Locate every blood parasite and identify its species.
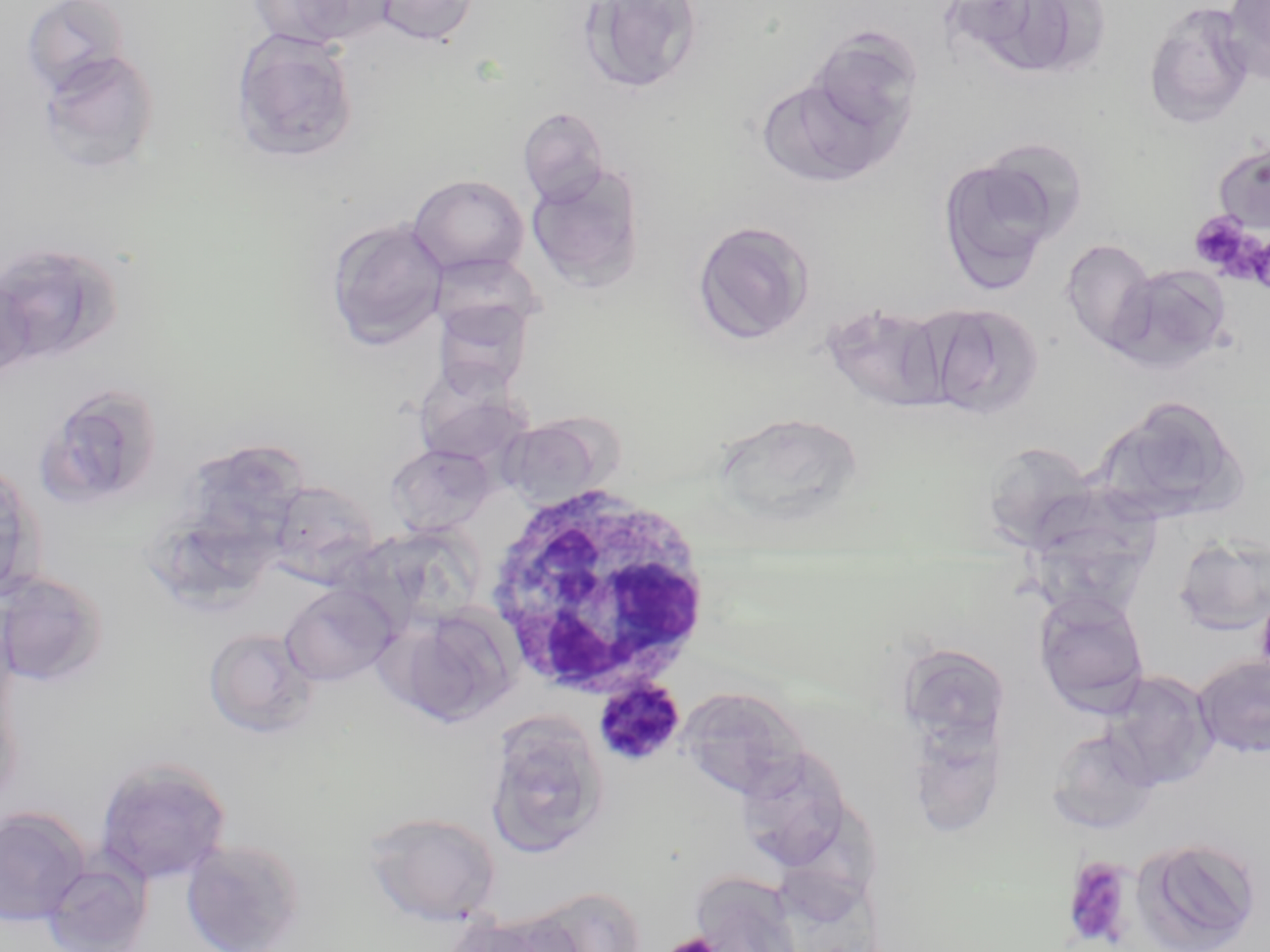
Approximate bounding boxes as (x1,y1)-(x2,y2) corner pairs in pixels.
Plasmodium malariae-infected red blood cells: (593,680)-(685,768).
No Plasmodium falciparum, Plasmodium ovale, Plasmodium vivax, Babesia divergens, or Trypanosoma brucei observed.

Uninfected red blood cell locations: (22,0)-(130,96), (251,0)-(394,49), (374,0)-(479,45), (579,0)-(705,95), (1221,0)-(1270,83), (1144,3)-(1255,128), (231,27)-(360,164), (805,29)-(923,142), (38,49)-(160,174), (757,75)-(902,189), (518,106)-(609,205), (979,136)-(1090,243), (1212,140)-(1270,234), (937,157)-(1059,294), (526,163)-(646,292), (408,174)-(529,277), (326,218)-(448,349), (692,219)-(815,345), (1060,238)-(1157,353), (0,241)-(124,365), (428,252)-(544,341), (1108,263)-(1234,374), (0,277)-(36,382), (432,298)-(535,397), (919,301)-(1046,420), (822,302)-(951,414), (36,382)-(164,509), (1094,395)-(1248,526), (503,417)-(607,509), (179,438)-(312,557), (979,441)-(1100,552), (387,443)-(494,535), (0,458)-(45,601), (265,480)-(381,584), (1172,534)-(1270,637), (0,571)-(109,687), (280,583)-(396,686), (1032,589)-(1151,718), (391,606)-(519,727), (203,627)-(317,737), (897,643)-(1012,751), (1193,653)-(1270,757), (1101,670)-(1218,790), (677,686)-(809,802), (907,707)-(1010,842), (483,711)-(610,859), (1046,727)-(1163,837), (733,746)-(857,871), (95,757)-(232,885), (0,807)-(90,926), (363,811)-(502,925), (1130,836)-(1262,952), (181,837)-(305,952), (41,859)-(152,952), (687,870)-(807,952), (520,885)-(647,952), (447,914)-(574,952). Platelet locations: (1189,212)-(1259,278), (1245,231)-(1270,293), (1062,856)-(1137,950), (663,933)-(720,952). White blood cell locations: (482,477)-(716,702). Slide-level diagnosis: Plasmodium malariae. May-Grünwald-Giemsa-stained preparation. Captured at 1000x magnification. Single field of view. Image is 1270×952 pixels. Light microscopy. Thin blood film.